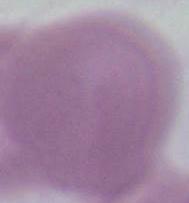 Captured at 1000x magnification. An erythrocyte is shown. Micrograph.